State which parasite is depicted.
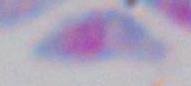

This is Toxoplasma gondii.

magnification = 1000x
modality = micrograph